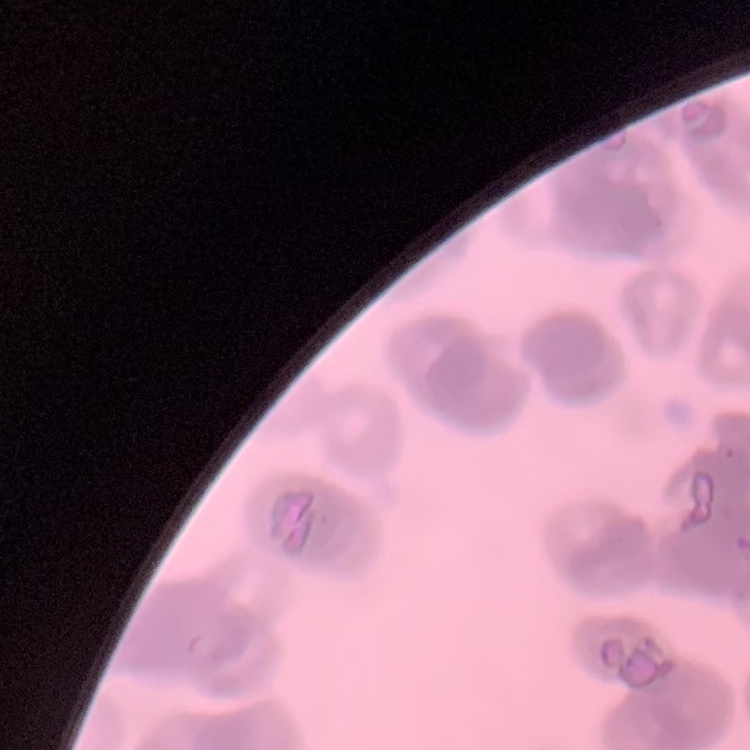 The red blood cells exhibit rouleaux formation. Square crop of a larger photomicrograph. Thin blood film. Stained with either Field's or Giemsa.